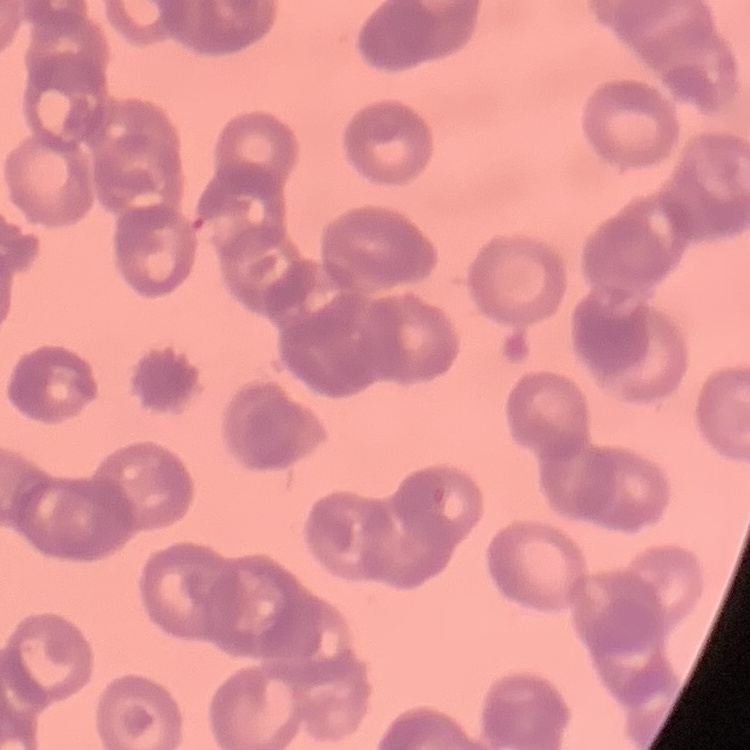

The red blood cells exhibit rouleaux formation. Square crop of a larger photomicrograph. Thin peripheral smear. Field's or Giemsa stain.